Classify this cell by malaria status.
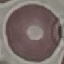
Uninfected.

Summary:
  - Image type: automatically extracted cell patch, resized to 64 × 64 pixels
  - Capture: smartphone camera at the microscope eyepiece
  - Stain: Giemsa
  - Preparation: thin blood smear